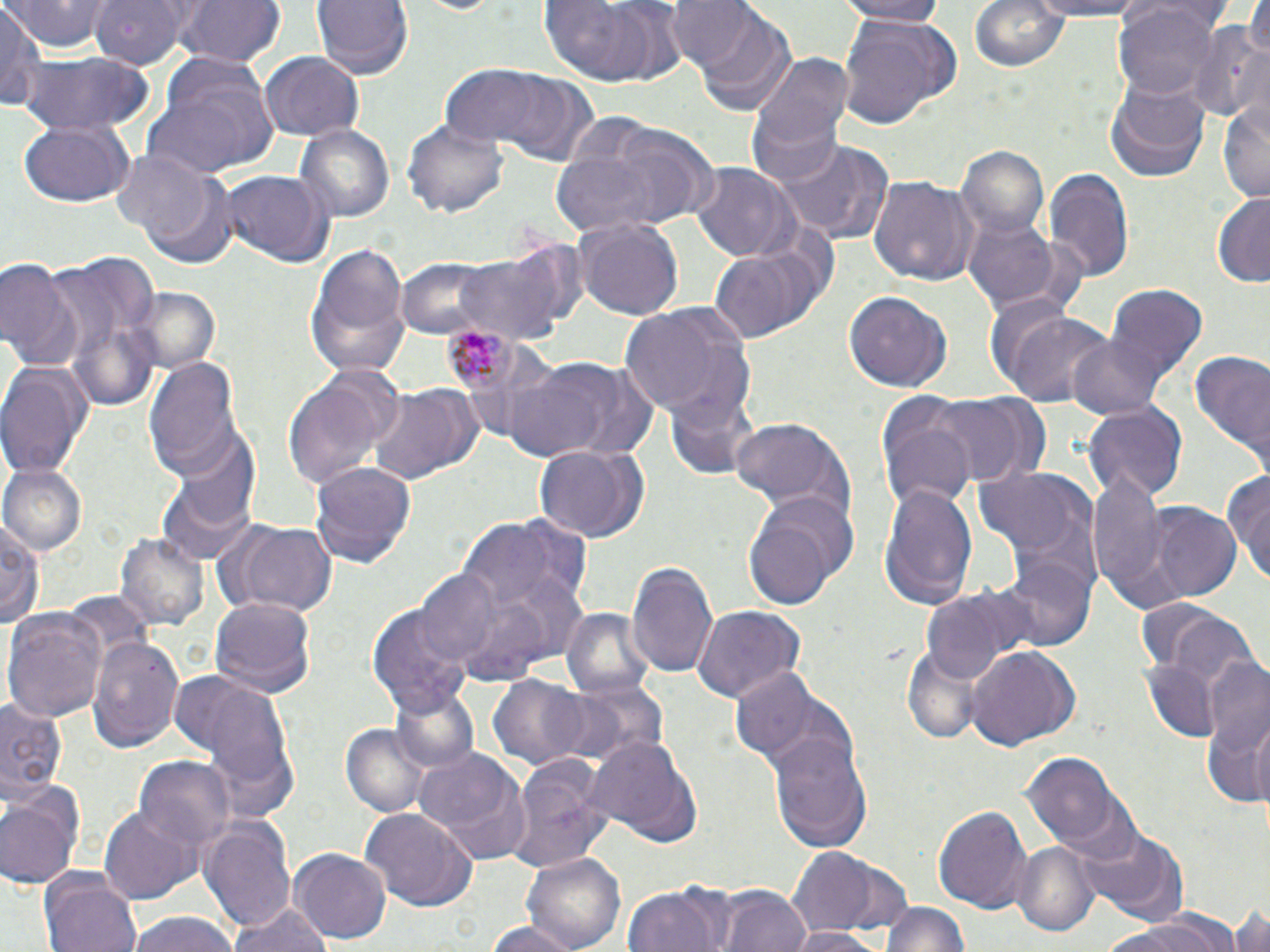
Summary:
  - Coordinate format: approximate bounding boxes as (x1, y1, x2, y2) in pixels
  - Uninfected red blood cell locations: (6, 0, 114, 52), (91, 0, 198, 68), (177, 0, 284, 70), (311, 0, 411, 79), (835, 0, 953, 24), (969, 0, 1072, 76), (1022, 0, 1151, 20), (540, 2, 656, 85), (664, 2, 763, 78), (0, 3, 45, 115), (1116, 4, 1220, 99), (685, 7, 799, 116), (835, 16, 956, 133), (1187, 22, 1270, 123), (17, 50, 154, 135), (742, 50, 855, 191), (260, 51, 364, 141), (145, 60, 279, 174), (439, 66, 553, 150), (476, 66, 603, 164), (1106, 80, 1210, 183), (1219, 96, 1270, 204), (402, 121, 507, 221), (17, 122, 133, 208), (576, 122, 718, 226), (293, 123, 396, 226), (777, 141, 894, 245), (959, 146, 1047, 240), (547, 153, 671, 241), (110, 155, 224, 262), (690, 164, 803, 264), (1043, 168, 1133, 278), (215, 170, 334, 267), (869, 175, 975, 288), (1211, 193, 1270, 286), (963, 217, 1059, 311), (573, 219, 684, 320), (455, 241, 580, 342), (709, 241, 823, 344), (303, 244, 410, 378), (41, 254, 158, 361), (0, 258, 81, 369), (395, 258, 504, 340), (1105, 286, 1207, 387), (128, 288, 221, 374), (844, 289, 951, 393), (622, 301, 756, 425), (995, 308, 1114, 411), (1066, 333, 1171, 422), (1185, 346, 1270, 467), (505, 352, 661, 466), (144, 355, 247, 482), (1, 361, 92, 477), (319, 365, 405, 448), (283, 382, 384, 491), (366, 384, 473, 488), (666, 389, 756, 482), (921, 394, 1034, 488), (877, 398, 978, 510), (1083, 404, 1189, 502), (728, 416, 852, 516), (170, 432, 262, 537), (534, 443, 652, 543), (310, 458, 418, 569), (2, 464, 86, 553), (1086, 464, 1174, 608), (973, 465, 1098, 572), (156, 469, 256, 568), (1225, 469, 1270, 584), (880, 480, 977, 605), (744, 499, 850, 609), (1150, 505, 1243, 602), (0, 512, 44, 631), (453, 518, 572, 617), (225, 521, 340, 618), (116, 531, 209, 633), (993, 558, 1096, 654), (627, 559, 717, 678), (417, 570, 501, 665), (922, 586, 1034, 681), (208, 596, 315, 698), (368, 604, 474, 723), (692, 605, 806, 705), (561, 606, 656, 702), (1150, 606, 1257, 686), (4, 609, 109, 723), (87, 633, 185, 753), (966, 646, 1082, 752), (901, 648, 987, 744), (1197, 651, 1270, 788), (1140, 659, 1221, 743), (728, 669, 835, 771), (179, 670, 297, 814), (487, 675, 593, 770), (560, 677, 668, 769), (390, 684, 480, 775), (0, 699, 66, 808), (1247, 717, 1270, 809), (342, 722, 432, 818), (768, 729, 873, 854), (583, 736, 707, 849), (414, 748, 533, 865), (503, 752, 615, 877), (1023, 753, 1122, 852), (135, 756, 237, 858), (0, 787, 82, 890), (931, 801, 1033, 916), (98, 803, 199, 906), (360, 806, 479, 912), (199, 816, 296, 932), (1072, 820, 1187, 924), (1014, 840, 1099, 936), (785, 846, 911, 940), (290, 848, 389, 945), (519, 852, 626, 952), (40, 869, 142, 952), (622, 886, 725, 952), (717, 886, 813, 952), (881, 900, 972, 952), (228, 901, 334, 952), (1231, 903, 1270, 952), (123, 912, 243, 952), (1101, 916, 1240, 952), (485, 920, 581, 952), (786, 926, 885, 952)
  - Plasmodium malariae-infected red blood cell locations: (436, 319, 523, 399)
  - Slide-level diagnosis: Plasmodium malariae
  - Preparation: thin blood film
  - Field of view: single
  - Magnification: 1000x
  - Modality: optical microscopy
  - Image size: 1270×952 pixels
  - Stain: May-Grünwald-Giemsa